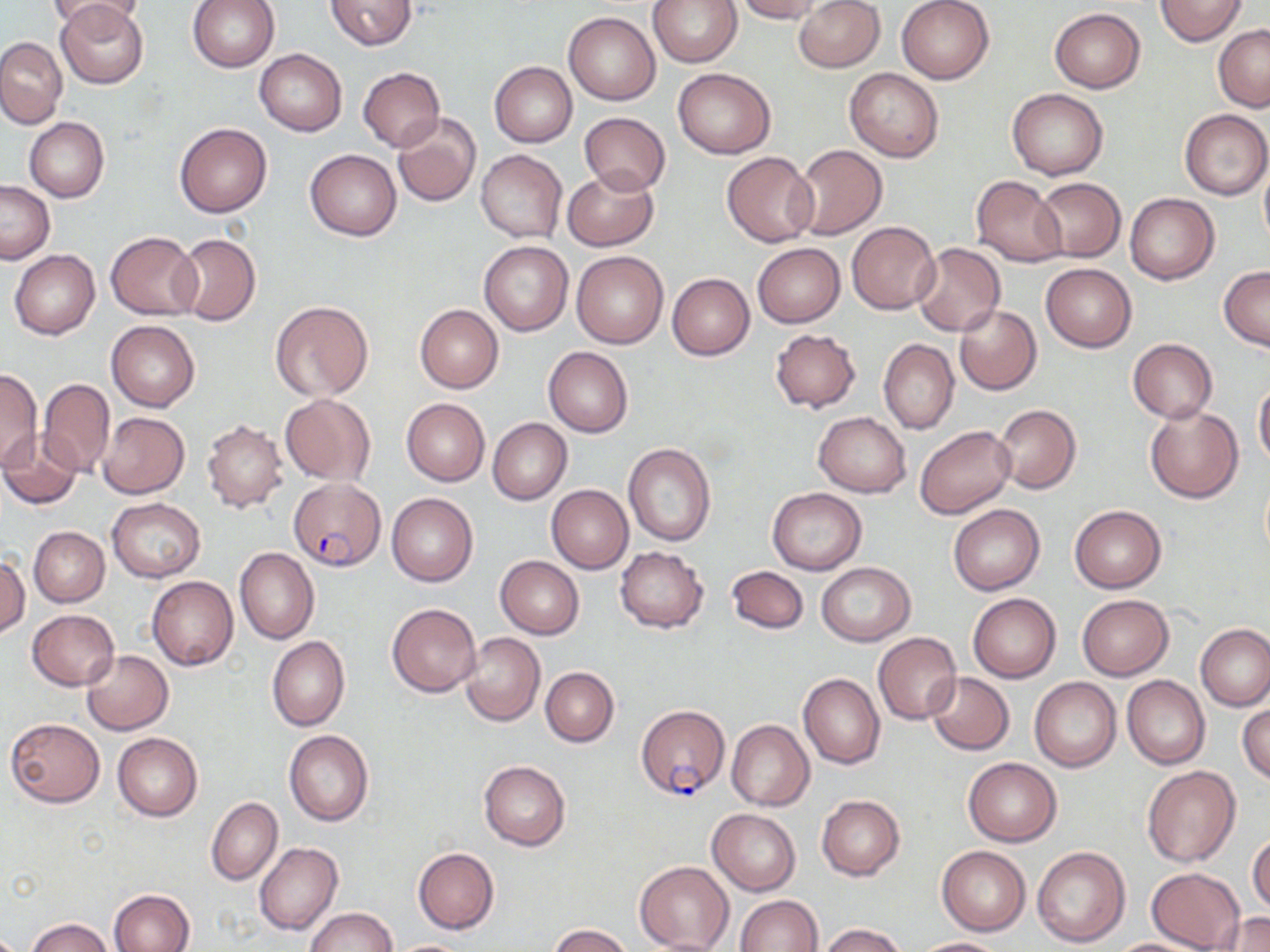
slide-level diagnosis = Plasmodium falciparum
magnification = 1000x
preparation = thin blood film
uninfected red blood cell locations = approximate bounding boxes as [x1, y1, x2, y2] in pixels: [47, 0, 145, 35], [187, 0, 280, 73], [326, 0, 416, 50], [648, 0, 742, 67], [734, 0, 826, 23], [896, 0, 995, 84], [1155, 0, 1248, 46], [793, 1, 884, 72], [55, 2, 149, 88], [1048, 8, 1145, 93], [563, 12, 660, 105], [1213, 25, 1270, 111], [0, 36, 66, 127], [254, 50, 347, 135], [489, 61, 577, 146], [358, 67, 445, 151], [673, 68, 776, 158], [844, 68, 944, 162], [1006, 87, 1108, 180], [1180, 109, 1269, 199], [579, 112, 670, 196], [391, 113, 482, 210], [25, 117, 108, 203], [176, 123, 272, 217], [794, 145, 887, 239], [305, 148, 401, 241], [475, 149, 567, 242], [721, 151, 818, 246], [1259, 158, 1270, 254], [561, 167, 658, 252], [970, 177, 1068, 266], [1033, 178, 1126, 262], [0, 181, 54, 263], [1125, 194, 1218, 283], [847, 221, 940, 313], [106, 232, 202, 320], [170, 234, 261, 326], [479, 241, 573, 335], [753, 243, 844, 327], [911, 243, 1005, 336], [9, 250, 100, 339], [572, 250, 668, 348], [1041, 263, 1136, 352], [1218, 266, 1270, 352], [667, 273, 754, 359], [270, 300, 373, 401], [415, 305, 503, 392], [954, 305, 1041, 394], [106, 320, 201, 411], [770, 328, 861, 413], [878, 337, 958, 434], [1127, 338, 1218, 422], [544, 347, 633, 438], [0, 369, 42, 471], [1254, 377, 1270, 472], [38, 378, 114, 477], [281, 394, 375, 484], [401, 398, 490, 486], [995, 405, 1080, 493], [1145, 405, 1243, 503], [814, 411, 911, 497], [97, 412, 190, 499], [488, 418, 571, 504], [201, 420, 288, 512], [915, 426, 1015, 518], [0, 430, 83, 510], [623, 443, 716, 546], [547, 485, 633, 573], [767, 487, 867, 574], [387, 493, 478, 586], [107, 498, 204, 581], [948, 503, 1044, 595], [1069, 504, 1167, 593], [28, 526, 109, 606], [616, 547, 708, 632], [235, 548, 320, 645], [1, 553, 30, 639], [496, 556, 584, 639], [816, 562, 916, 646], [726, 566, 808, 633], [147, 576, 238, 670], [968, 592, 1061, 683], [1077, 594, 1173, 679], [386, 603, 481, 697], [27, 609, 119, 690], [1196, 624, 1270, 710], [461, 632, 545, 727], [873, 632, 962, 725], [268, 636, 349, 732], [82, 650, 174, 735], [540, 666, 619, 747], [926, 672, 1014, 755], [800, 673, 885, 769], [1122, 675, 1210, 769], [1029, 678, 1121, 772], [1238, 700, 1269, 785], [5, 718, 105, 807], [726, 719, 814, 811], [284, 730, 373, 826], [112, 732, 202, 820], [963, 757, 1062, 846], [479, 760, 571, 850], [1142, 766, 1241, 868], [817, 795, 905, 880], [207, 797, 282, 885], [707, 809, 801, 895], [1248, 833, 1270, 914], [254, 842, 343, 935], [937, 845, 1030, 936], [1032, 846, 1131, 948], [413, 848, 499, 933], [634, 861, 734, 950], [1146, 867, 1245, 952], [108, 889, 195, 952], [734, 895, 822, 952], [307, 907, 396, 952], [1217, 913, 1270, 951], [27, 917, 112, 952], [819, 923, 906, 952], [549, 924, 631, 951], [914, 937, 1007, 952], [1106, 937, 1210, 951], [385, 939, 477, 952]
modality = optical microscopy
Plasmodium falciparum-infected red blood cell locations = approximate bounding boxes as [x1, y1, x2, y2] in pixels: [289, 478, 384, 573], [636, 705, 730, 800]
stain = May-Grünwald-Giemsa
image size = 1270×952 pixels
field of view = one of a larger specimen